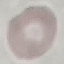
malaria status = uninfected
preparation = thin blood smear
capture = smartphone camera at the microscope eyepiece
image type = automatically extracted cell patch, resized to 64 × 64 pixels
stain = Giemsa